Report the malaria status of this cell.
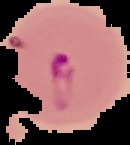
It is parasitized.

{
  "image_size": "130×145 pixels",
  "image_type": "segmented cell region on a black background",
  "preparation": "thin blood smear"
}